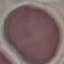 Malaria status: uninfected. Cell patch, automatically extracted from a larger field of view and resized to 64 × 64 pixels. Thin blood smear. Giemsa-stained preparation. Photographed with a smartphone camera at the microscope eyepiece.